Assess this cell for malaria.
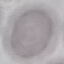

Uninfected.

Giemsa stain. Acquired by smartphone through the microscope eyepiece. Automatically extracted cell patch, resized to 64 × 64 pixels. Thin smear of blood.